Assess this cell for malaria.
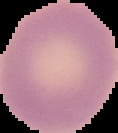

It is uninfected.

image size = 118×133 pixels
image type = segmented cell region with the area outside set to black
preparation = thin blood smear